Locate every Plasmodium falciparum-infected red blood cell.
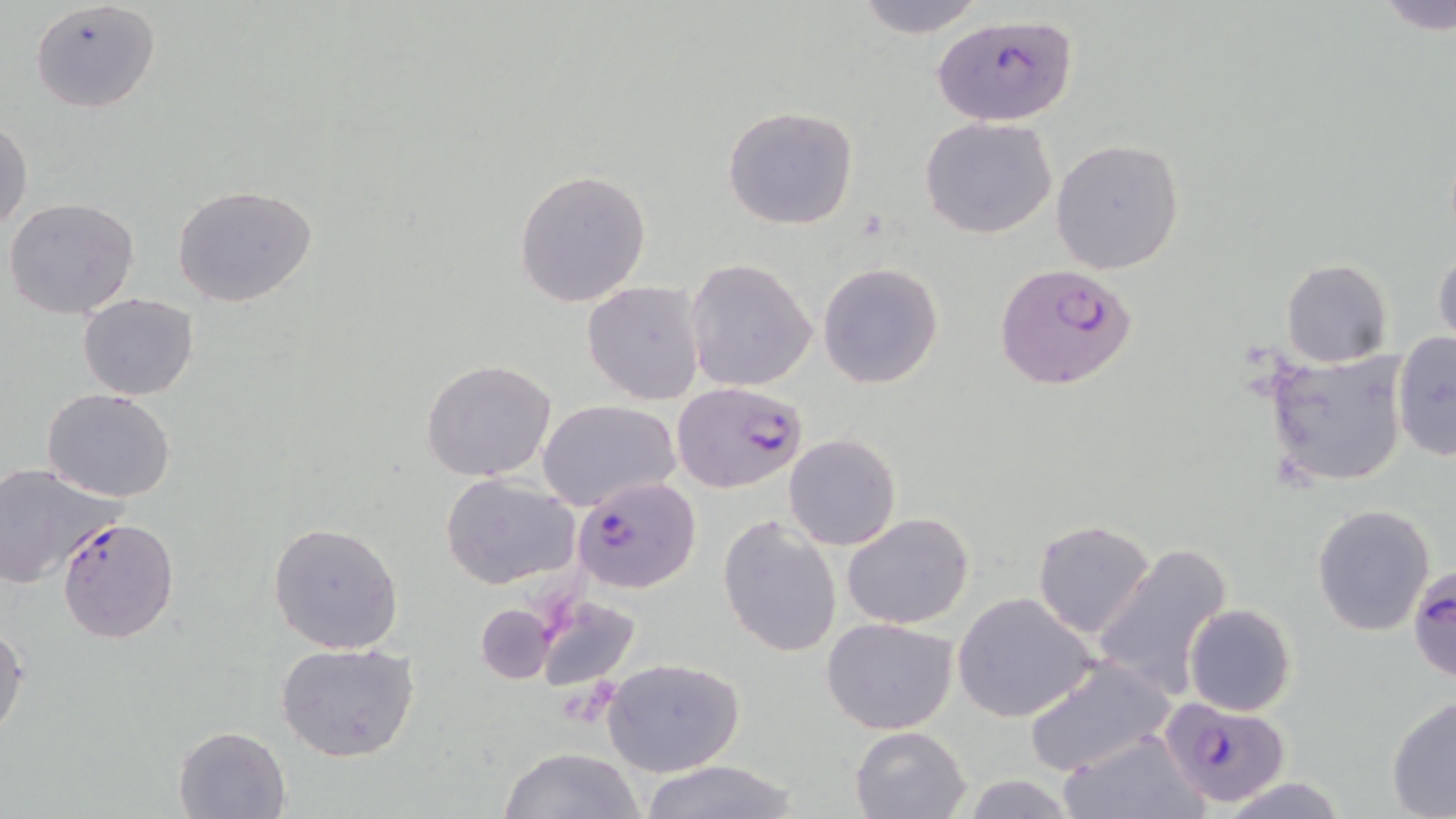
Approximate bounding boxes as (x1,y1)-(x2,y2) corner pairs in pixels.
Plasmodium falciparum-infected red blood cells: (930,13)-(1080,128), (994,264)-(1138,391), (671,381)-(809,494), (572,476)-(702,594), (56,516)-(180,645), (1409,565)-(1455,686), (1158,698)-(1290,806).

Summary:
  - Uninfected red blood cell locations: (30,0)-(160,112), (851,0)-(985,39), (1375,0)-(1456,35), (722,105)-(859,230), (920,117)-(1058,240), (0,118)-(32,234), (1049,138)-(1184,275), (514,169)-(652,308), (171,184)-(316,308), (4,198)-(139,319), (1433,244)-(1455,351), (685,258)-(817,393), (1281,259)-(1392,367), (817,263)-(944,388), (583,281)-(705,404), (78,292)-(199,400), (1392,333)-(1456,461), (1263,348)-(1408,489), (422,359)-(557,482), (41,387)-(178,502), (536,400)-(680,509), (783,434)-(902,551), (0,463)-(123,587), (439,472)-(582,590), (1312,503)-(1436,636), (841,512)-(975,630), (717,514)-(841,659), (1032,519)-(1157,639), (268,520)-(404,653), (1090,542)-(1233,702), (952,592)-(1099,723), (534,596)-(642,691), (475,603)-(554,685), (1185,604)-(1296,717), (822,617)-(959,735), (0,620)-(27,741), (274,642)-(420,762), (603,656)-(745,777), (1021,656)-(1174,777), (1386,696)-(1456,817), (173,725)-(292,817), (849,727)-(972,818), (1062,733)-(1204,818), (498,746)-(645,819), (638,760)-(802,819), (954,776)-(1083,818), (1217,776)-(1349,818)
  - Slide-level diagnosis: Plasmodium falciparum
  - Preparation: thin blood film
  - Magnification: 1000x
  - Stain: May-Grünwald-Giemsa
  - Image size: 1456×819 pixels
  - Modality: light microscopy
  - Field of view: one of a larger specimen